Give the extent of all Plasmodium falciparum-infected red blood cells.
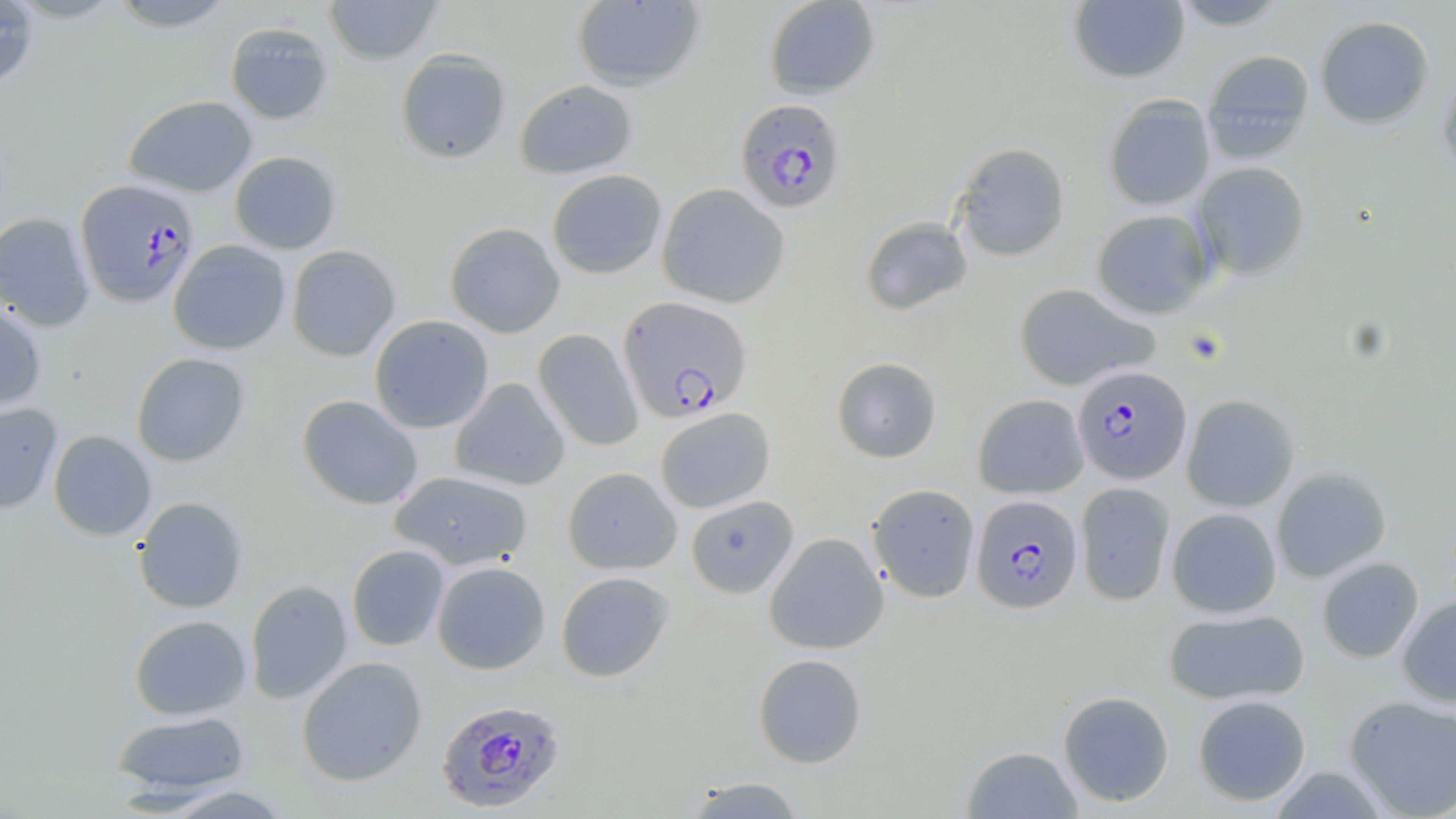

Approximate bounding boxes as (x1,y1)-(x2,y2) corner pairs in pixels.
Plasmodium falciparum-infected red blood cells: (735,98)-(848,214), (75,178)-(200,307), (618,295)-(752,423), (1072,365)-(1192,484), (971,494)-(1083,614), (436,698)-(566,814).

slide-level diagnosis = Plasmodium falciparum
preparation = thin blood film
modality = light microscopy
image size = 1456×819 pixels
uninfected red blood cell locations = approximate bounding boxes as (x1,y1)-(x2,y2) corner pairs in pixels: (108,0)-(237,32), (324,0)-(443,65), (764,0)-(880,99), (1169,0)-(1292,31), (0,1)-(39,89), (572,1)-(705,91), (1069,1)-(1190,84), (1315,15)-(1435,129), (225,21)-(334,126), (395,49)-(511,164), (1202,49)-(1315,163), (1437,70)-(1456,188), (515,79)-(638,179), (124,95)-(257,197), (1103,95)-(1216,211), (952,142)-(1070,261), (229,150)-(342,254), (1193,161)-(1310,280), (546,169)-(667,279), (657,183)-(790,308), (1091,209)-(1215,319), (0,213)-(95,332), (860,217)-(973,315), (445,222)-(565,338), (168,239)-(291,355), (286,245)-(401,361), (1014,283)-(1159,391), (0,301)-(47,413), (369,315)-(494,433), (533,328)-(643,451), (131,352)-(250,467), (832,357)-(942,463), (449,378)-(570,491), (972,393)-(1089,499), (297,394)-(423,510), (1182,394)-(1300,512), (0,402)-(63,514), (654,407)-(775,513), (48,430)-(156,541), (563,467)-(682,574), (1271,467)-(1391,582), (389,470)-(534,571), (867,482)-(980,602), (1075,482)-(1175,606), (685,495)-(799,598), (133,496)-(248,613), (1167,507)-(1282,618), (764,532)-(888,654), (347,544)-(450,651), (1317,557)-(1424,663), (431,561)-(550,674), (556,571)-(675,682), (245,579)-(352,704), (1397,596)-(1456,707), (1163,608)-(1309,705), (129,614)-(252,720), (753,653)-(868,768), (297,656)-(427,786), (1057,690)-(1175,807), (1193,694)-(1311,806), (1343,695)-(1456,818), (111,710)-(252,801), (961,745)-(1084,818), (681,774)-(808,818), (155,784)-(295,818)
field of view = single
stain = May-Grünwald-Giemsa
magnification = 1000x